Point out each leukocyte.
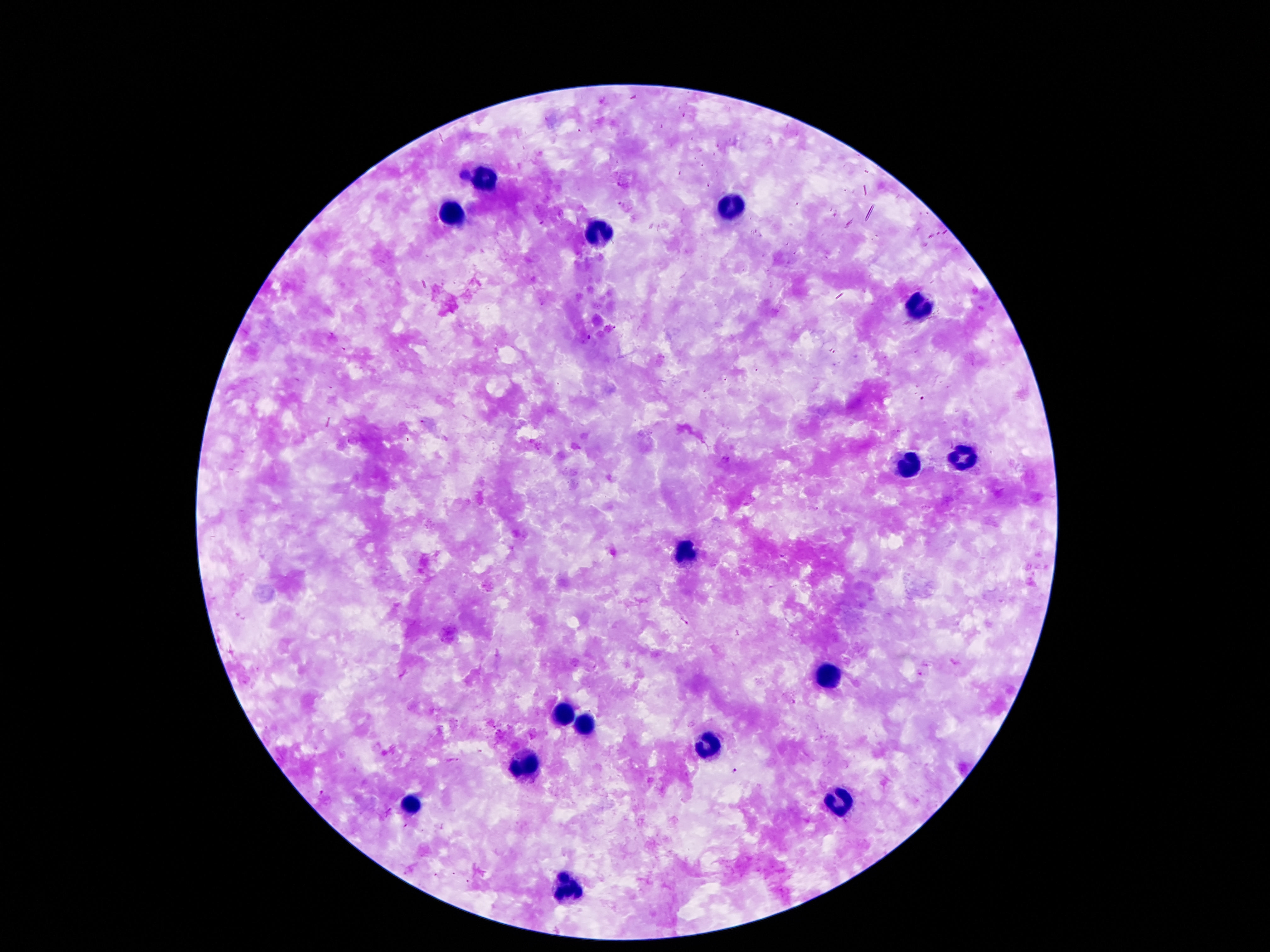

Approximate centers as (x, y) in pixels.
Leukocytes: (482, 176), (728, 208), (455, 215), (591, 232), (921, 306), (963, 455), (906, 464), (688, 555), (829, 676), (564, 709), (583, 724), (711, 747), (526, 764), (413, 804), (837, 804), (568, 887).

Summary:
  - Patient malaria status: not infected
  - Preparation: thick peripheral-blood smear
  - Image size: 1270×952 pixels
  - Field of view: single
  - Magnification: 100x
  - Capture: smartphone camera through the microscope eyepiece
  - Stain: Giemsa